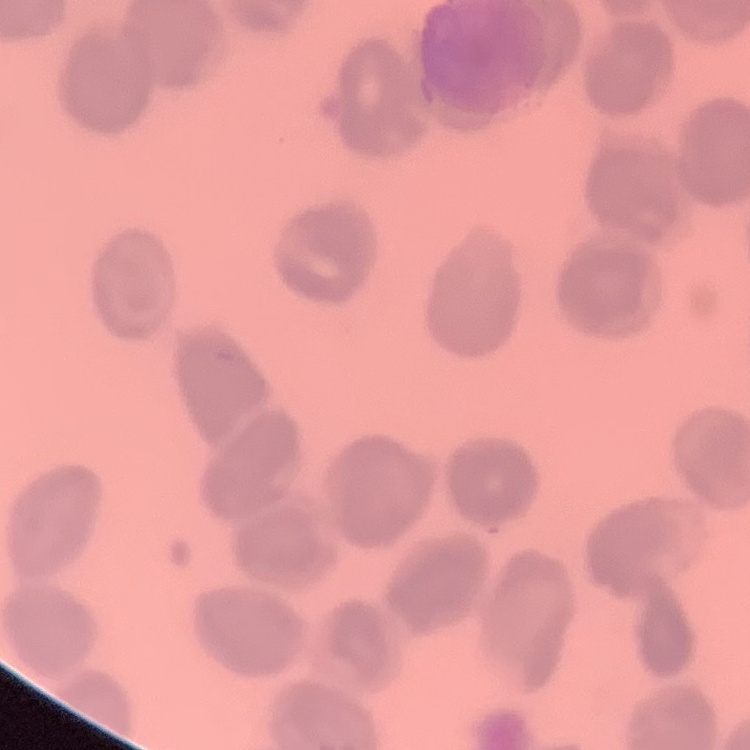

red blood cell morphology = no rouleaux formation
image type = one tile cut from a larger photomicrograph
stain = Field's or Giemsa
preparation = thin blood smear